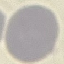
malaria status = uninfected
capture = smartphone through the microscope eyepiece
stain = Giemsa
preparation = thin smear
image type = cell patch, automatically extracted from a larger field of view and resized to 64 × 64 pixels